Locate every Plasmodium vivax-infected red blood cell.
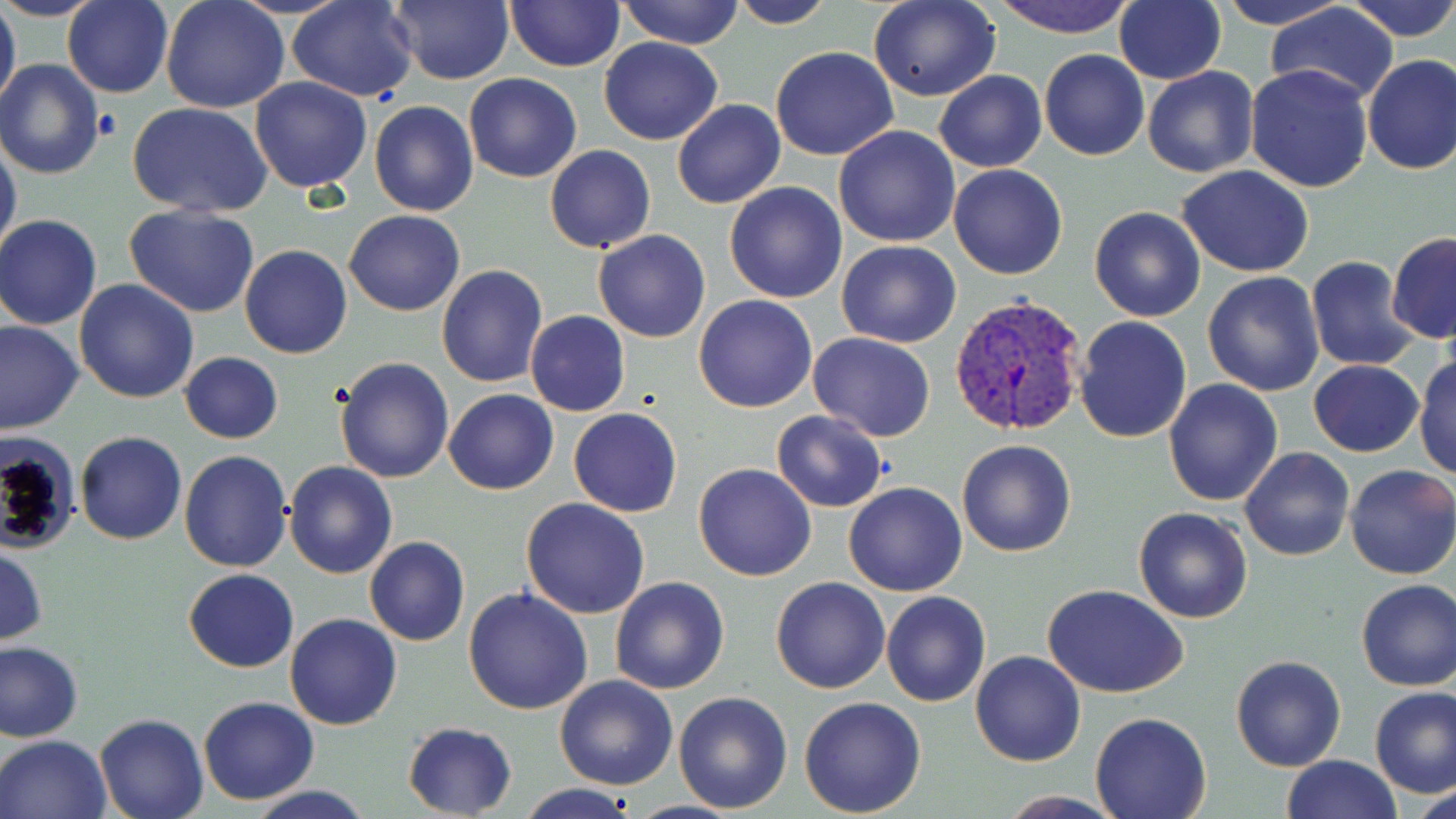
Approximate bounding boxes as named x1/y1/x2/y2 corners in pixels.
Plasmodium vivax-infected red blood cells: (x1=949, y1=292, x2=1090, y2=436).

Summary:
  - Platelet locations: (x1=92, y1=108, x2=122, y2=140)
  - Uninfected red blood cell locations: (x1=0, y1=0, x2=109, y2=21), (x1=0, y1=0, x2=21, y2=118), (x1=63, y1=0, x2=173, y2=99), (x1=286, y1=0, x2=419, y2=101), (x1=389, y1=0, x2=511, y2=86), (x1=618, y1=0, x2=744, y2=48), (x1=728, y1=0, x2=836, y2=28), (x1=869, y1=0, x2=1001, y2=102), (x1=988, y1=0, x2=1137, y2=39), (x1=1213, y1=0, x2=1355, y2=30), (x1=1345, y1=0, x2=1456, y2=41), (x1=161, y1=1, x2=290, y2=113), (x1=505, y1=1, x2=623, y2=71), (x1=1115, y1=1, x2=1225, y2=84), (x1=1267, y1=3, x2=1398, y2=106), (x1=598, y1=36, x2=724, y2=146), (x1=771, y1=46, x2=900, y2=161), (x1=1040, y1=49, x2=1150, y2=160), (x1=1361, y1=53, x2=1456, y2=175), (x1=0, y1=59, x2=105, y2=179), (x1=1244, y1=64, x2=1375, y2=193), (x1=1142, y1=65, x2=1261, y2=179), (x1=935, y1=69, x2=1047, y2=173), (x1=463, y1=72, x2=582, y2=182), (x1=249, y1=75, x2=372, y2=194), (x1=671, y1=98, x2=786, y2=208), (x1=368, y1=100, x2=479, y2=218), (x1=127, y1=103, x2=272, y2=218), (x1=834, y1=126, x2=960, y2=247), (x1=0, y1=137, x2=22, y2=262), (x1=545, y1=145, x2=656, y2=252), (x1=948, y1=164, x2=1068, y2=279), (x1=1178, y1=167, x2=1316, y2=276), (x1=724, y1=181, x2=847, y2=304), (x1=124, y1=204, x2=260, y2=316), (x1=1089, y1=206, x2=1206, y2=322), (x1=344, y1=209, x2=465, y2=316), (x1=0, y1=215, x2=103, y2=328), (x1=592, y1=230, x2=712, y2=343), (x1=1387, y1=232, x2=1456, y2=344), (x1=837, y1=239, x2=961, y2=348), (x1=240, y1=245, x2=352, y2=360), (x1=1305, y1=256, x2=1421, y2=371), (x1=437, y1=264, x2=549, y2=387), (x1=1202, y1=270, x2=1325, y2=396), (x1=74, y1=279, x2=200, y2=404), (x1=694, y1=294, x2=818, y2=412), (x1=525, y1=310, x2=630, y2=417), (x1=1074, y1=314, x2=1192, y2=442), (x1=0, y1=321, x2=84, y2=436), (x1=806, y1=333, x2=937, y2=441), (x1=180, y1=352, x2=283, y2=443), (x1=1413, y1=352, x2=1456, y2=480), (x1=334, y1=355, x2=455, y2=483), (x1=1309, y1=360, x2=1425, y2=457), (x1=1163, y1=378, x2=1283, y2=507), (x1=443, y1=388, x2=559, y2=495), (x1=568, y1=407, x2=682, y2=517), (x1=770, y1=409, x2=888, y2=511), (x1=75, y1=431, x2=188, y2=544), (x1=0, y1=434, x2=83, y2=558), (x1=956, y1=438, x2=1076, y2=557), (x1=1241, y1=447, x2=1355, y2=562), (x1=179, y1=451, x2=292, y2=573), (x1=282, y1=461, x2=398, y2=580), (x1=694, y1=463, x2=817, y2=583), (x1=1345, y1=464, x2=1456, y2=580), (x1=843, y1=482, x2=967, y2=596), (x1=520, y1=497, x2=651, y2=620), (x1=1133, y1=507, x2=1254, y2=624), (x1=364, y1=536, x2=470, y2=646), (x1=0, y1=545, x2=48, y2=647), (x1=183, y1=569, x2=299, y2=672), (x1=609, y1=576, x2=729, y2=694), (x1=771, y1=576, x2=892, y2=693), (x1=1355, y1=577, x2=1456, y2=690), (x1=1045, y1=585, x2=1188, y2=698), (x1=464, y1=586, x2=594, y2=716), (x1=881, y1=591, x2=992, y2=708), (x1=285, y1=613, x2=402, y2=729), (x1=0, y1=641, x2=83, y2=742), (x1=969, y1=650, x2=1086, y2=767), (x1=1230, y1=655, x2=1346, y2=771), (x1=553, y1=675, x2=678, y2=790), (x1=1371, y1=688, x2=1456, y2=798), (x1=673, y1=690, x2=794, y2=813), (x1=198, y1=696, x2=321, y2=805), (x1=799, y1=696, x2=927, y2=816), (x1=1090, y1=712, x2=1213, y2=819), (x1=94, y1=713, x2=208, y2=819), (x1=402, y1=721, x2=519, y2=816), (x1=0, y1=733, x2=111, y2=819), (x1=1280, y1=754, x2=1402, y2=818), (x1=244, y1=784, x2=377, y2=819), (x1=516, y1=784, x2=640, y2=818), (x1=1408, y1=785, x2=1455, y2=819), (x1=995, y1=790, x2=1124, y2=818)
  - Slide-level diagnosis: Plasmodium vivax
  - Magnification: 1000x
  - Image size: 1456×819 pixels
  - Stain: May-Grünwald-Giemsa
  - Preparation: thin blood film
  - Modality: light microscopy
  - Field of view: one of a larger specimen